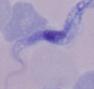

Summary:
  - Magnification: 1000x
  - Modality: micrograph
  - Identification: trypanosome